State which cell type is depicted.
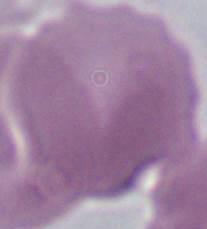
An erythrocyte.

Captured at 1000x magnification. Photomicrograph.